Locate every leukocyte (white blood cell).
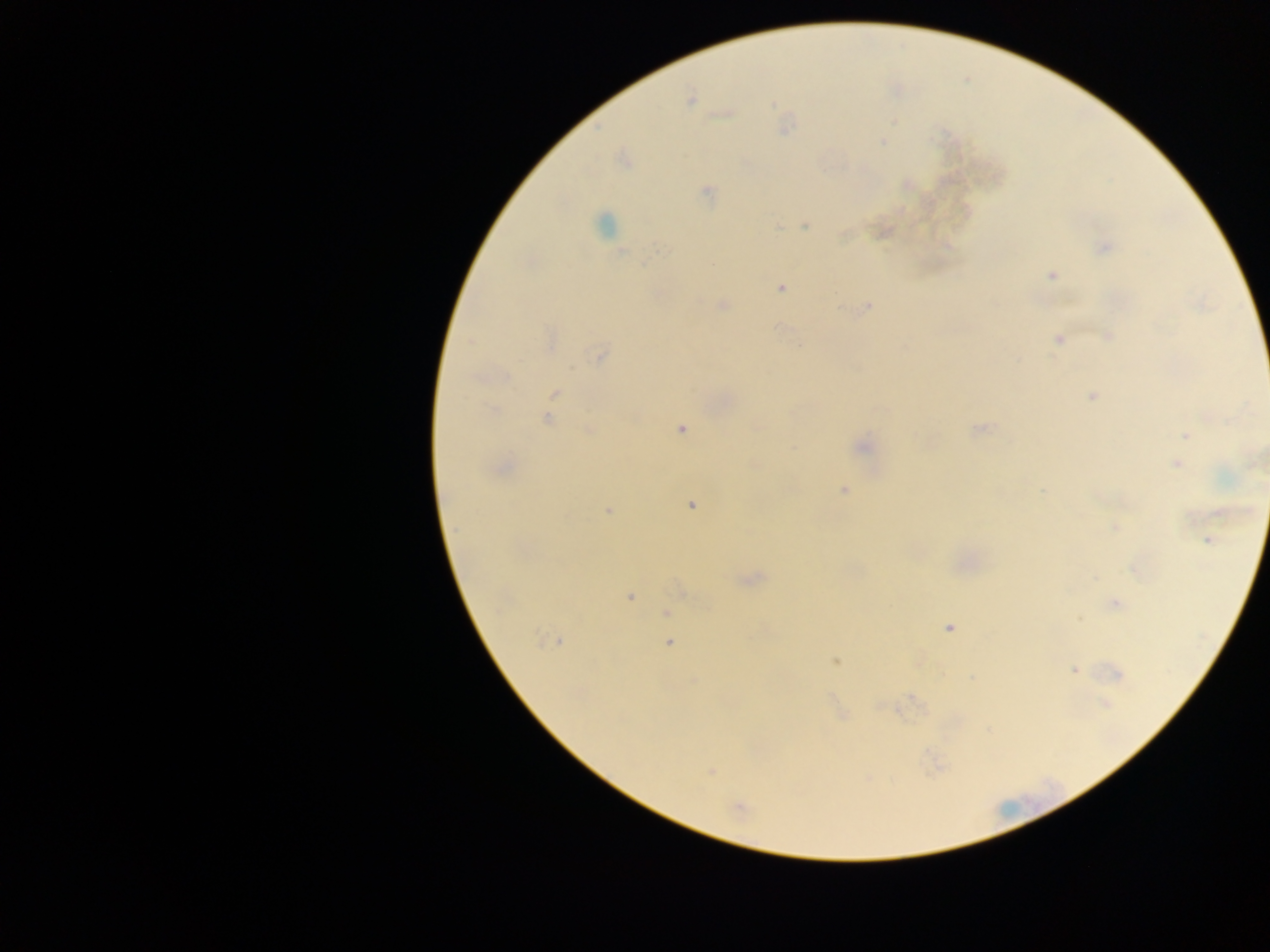

No leukocytes observed.

image size = 1270×952 pixels
field of view = single
preparation = thick blood smear
capture = mobile-phone photograph through a microscope
country = Ghana
malaria parasite locations = approximate centers as [x, y] in pixels: [689, 100], [883, 142], [708, 192], [604, 223], [778, 227], [806, 227], [1104, 247], [660, 251], [621, 253], [712, 265], [1051, 275], [780, 288], [723, 305], [868, 306], [1107, 336], [1058, 339], [550, 340], [470, 341], [600, 355], [506, 376], [555, 393], [1091, 396], [493, 410], [547, 419], [681, 429], [978, 429], [589, 430], [1185, 436], [862, 447], [1176, 464], [502, 467], [844, 491], [1042, 491], [691, 505], [608, 510], [1115, 527], [1207, 541], [751, 579], [630, 597], [1115, 603], [667, 613], [1079, 619], [949, 628], [557, 642], [668, 644], [835, 661], [1073, 670], [1117, 674], [693, 681], [1105, 703], [710, 771], [739, 809]